Classify this cell by malaria status.
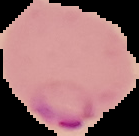
Parasitized.

Summary:
  - Preparation: thin blood film
  - Image size: 139×136 pixels
  - Image type: segmented cell region on a black background